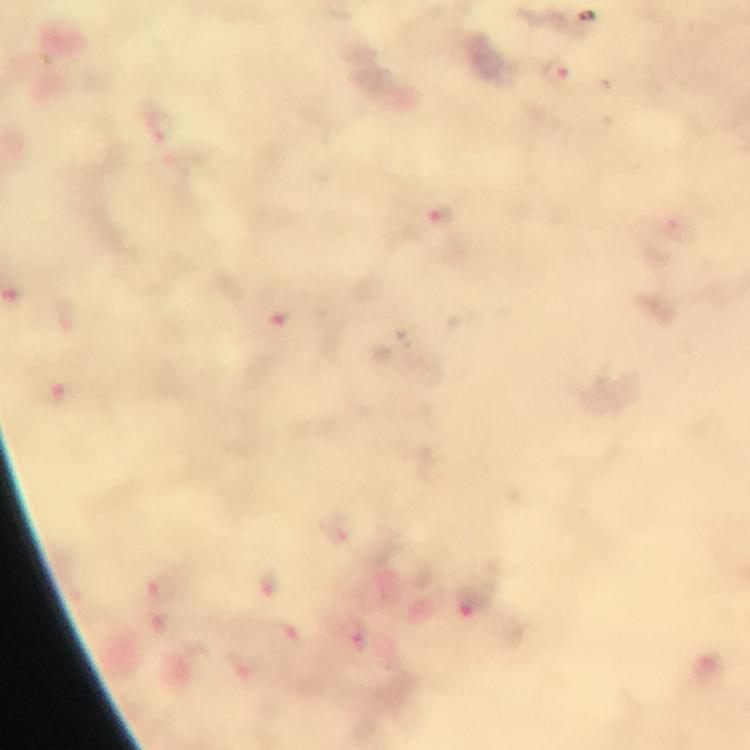 Approximate centers as (x, y) in pixels. Plasmodium parasite locations: (556, 75), (440, 216). Photographed through the microscope with a smartphone camera. 100x magnification. Giemsa-stained preparation. Image is 750×750 pixels. From a diagnostic examination for malaria. A crop from one field of view. Immersion oil was used. Thick blood smear.